Report the malaria status of this cell.
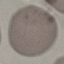

Uninfected.

Summary:
  - Image type: cell patch, automatically extracted from a larger field of view and resized to 64 × 64 pixels
  - Stain: Giemsa
  - Capture: smartphone camera at the microscope eyepiece
  - Preparation: thin blood smear